Assess this cell for malaria.
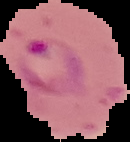

Parasitized.

{
  "preparation": "thin blood smear",
  "image_size": "130×142 pixels",
  "image_type": "cell region segmented out of the field of view; surrounding area masked to black"
}